Give the position of every Plasmodium parasite and every leukocyte.
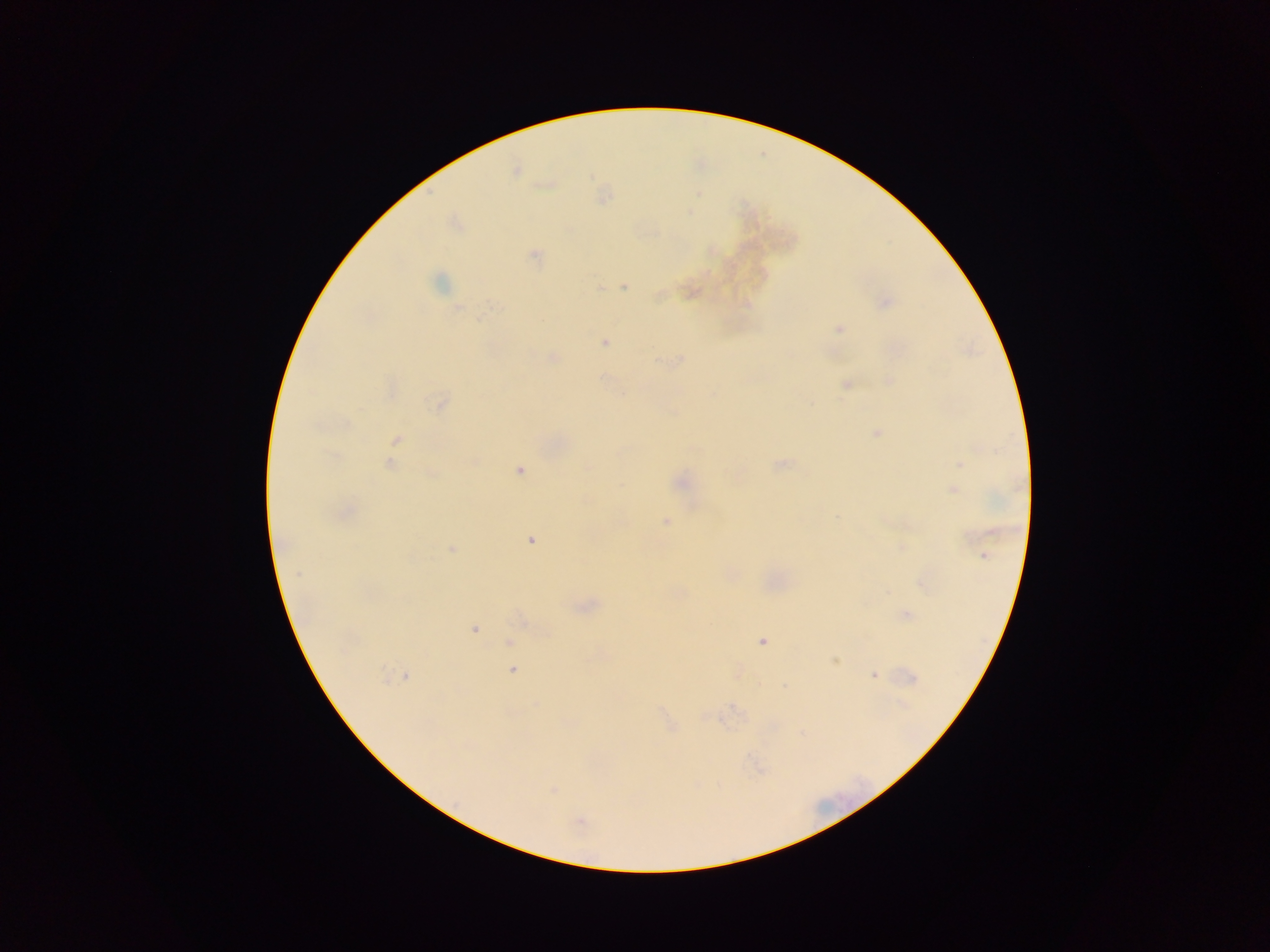
Approximate centers as {x, y} in pixels.
Plasmodium parasites: {515, 171}, {534, 255}, {439, 282}, {623, 286}, {599, 288}, {659, 295}, {886, 302}, {457, 308}, {479, 318}, {838, 328}, {604, 342}, {553, 358}, {889, 381}, {846, 384}, {623, 395}, {439, 404}, {877, 433}, {397, 439}, {782, 463}, {390, 464}, {960, 464}, {588, 468}, {520, 470}, {432, 474}, {681, 482}, {953, 490}, {836, 516}, {665, 521}, {530, 541}, {452, 548}, {902, 548}, {984, 556}, {299, 573}, {907, 615}, {474, 629}, {762, 642}, {509, 643}, {835, 661}, {512, 670}, {874, 675}, {406, 676}, {913, 679}, {785, 686}, {903, 705}, {735, 708}, {553, 791}, {580, 824}.
No leukocytes observed.

Summary:
  - Preparation: thick blood smear
  - Capture: mobile-phone photograph through a microscope
  - Field of view: single
  - Image size: 1270×952 pixels
  - Country: Ghana